Outline each blood parasite and name the species.
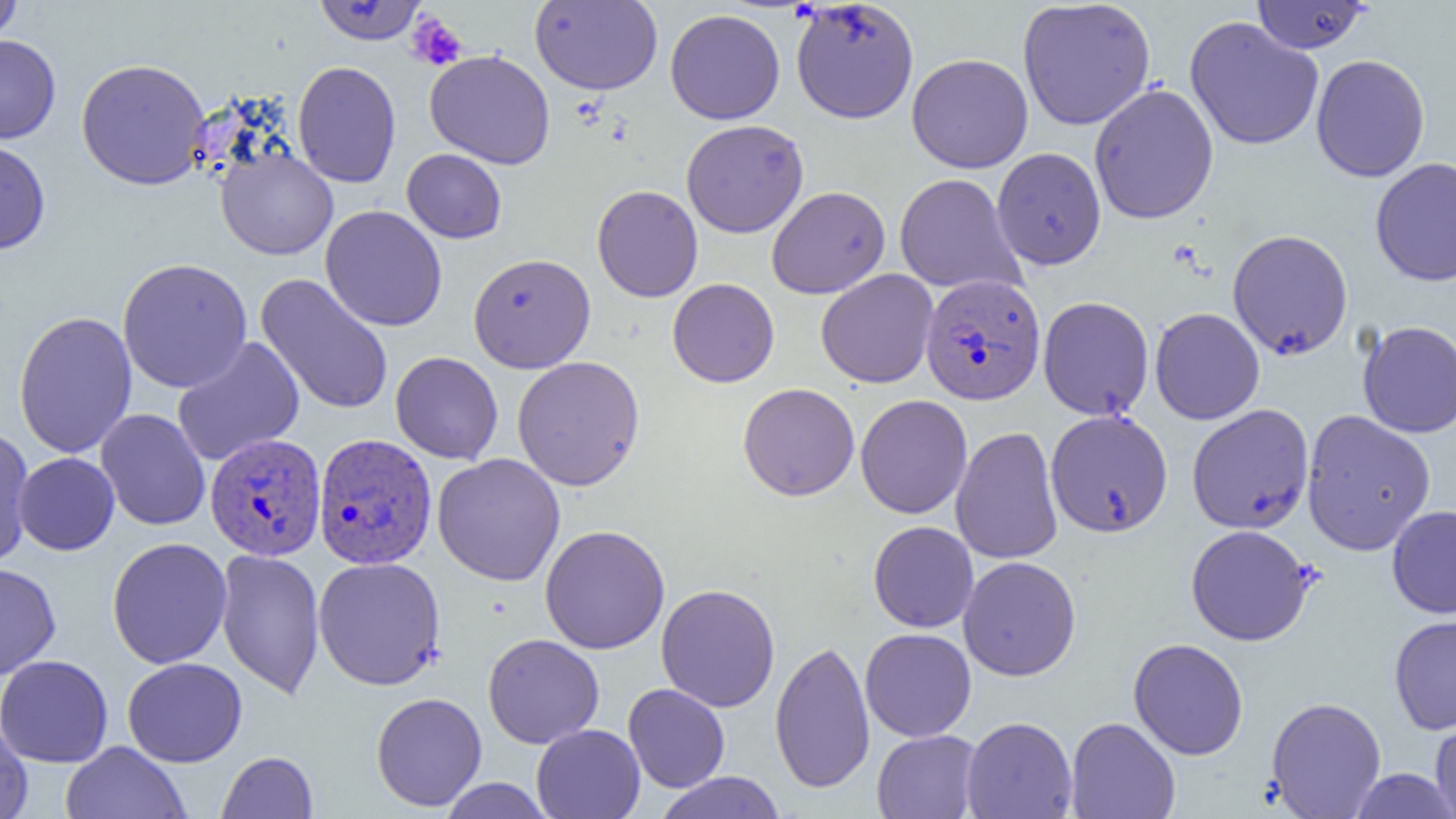

Approximate bounding boxes as named x1/y1/x2/y2 corners in pixels.
Plasmodium vivax-infected red blood cells: (x1=920, y1=274, x2=1046, y2=405), (x1=205, y1=433, x2=327, y2=561), (x1=313, y1=433, x2=437, y2=569).
No Plasmodium falciparum, Plasmodium ovale, Plasmodium malariae, Babesia divergens, or Trypanosoma brucei observed.

Uninfected red blood cell locations: (x1=0, y1=0, x2=22, y2=46), (x1=312, y1=0, x2=427, y2=44), (x1=530, y1=0, x2=663, y2=95), (x1=791, y1=1, x2=919, y2=123), (x1=1017, y1=1, x2=1156, y2=130), (x1=1250, y1=1, x2=1370, y2=53), (x1=665, y1=9, x2=785, y2=125), (x1=1184, y1=17, x2=1324, y2=150), (x1=0, y1=34, x2=61, y2=144), (x1=425, y1=50, x2=555, y2=170), (x1=906, y1=53, x2=1033, y2=173), (x1=1310, y1=54, x2=1430, y2=182), (x1=76, y1=58, x2=211, y2=190), (x1=292, y1=61, x2=402, y2=188), (x1=1089, y1=83, x2=1219, y2=224), (x1=681, y1=119, x2=809, y2=238), (x1=0, y1=138, x2=51, y2=255), (x1=216, y1=147, x2=338, y2=260), (x1=991, y1=147, x2=1106, y2=270), (x1=402, y1=149, x2=507, y2=243), (x1=1370, y1=157, x2=1456, y2=287), (x1=894, y1=173, x2=1025, y2=295), (x1=592, y1=185, x2=703, y2=302), (x1=767, y1=186, x2=891, y2=299), (x1=320, y1=205, x2=448, y2=331), (x1=1227, y1=228, x2=1353, y2=360), (x1=468, y1=252, x2=596, y2=373), (x1=117, y1=257, x2=253, y2=393), (x1=815, y1=269, x2=939, y2=388), (x1=256, y1=273, x2=395, y2=416), (x1=668, y1=278, x2=779, y2=387), (x1=1038, y1=296, x2=1154, y2=421), (x1=1150, y1=307, x2=1265, y2=424), (x1=13, y1=311, x2=138, y2=459), (x1=1357, y1=321, x2=1456, y2=437), (x1=172, y1=337, x2=305, y2=466), (x1=390, y1=351, x2=503, y2=464), (x1=512, y1=355, x2=645, y2=491), (x1=737, y1=383, x2=859, y2=500), (x1=855, y1=395, x2=972, y2=518), (x1=1187, y1=404, x2=1314, y2=534), (x1=96, y1=409, x2=211, y2=531), (x1=1045, y1=409, x2=1173, y2=537), (x1=1301, y1=410, x2=1436, y2=555), (x1=951, y1=426, x2=1064, y2=565), (x1=1, y1=428, x2=35, y2=565), (x1=13, y1=452, x2=119, y2=555), (x1=432, y1=453, x2=565, y2=586), (x1=1387, y1=505, x2=1456, y2=618), (x1=868, y1=521, x2=978, y2=633), (x1=540, y1=524, x2=670, y2=654), (x1=1185, y1=524, x2=1316, y2=646), (x1=106, y1=536, x2=232, y2=669), (x1=216, y1=548, x2=325, y2=700), (x1=959, y1=556, x2=1081, y2=681), (x1=313, y1=557, x2=446, y2=691), (x1=0, y1=563, x2=61, y2=679), (x1=656, y1=583, x2=780, y2=712), (x1=1389, y1=613, x2=1456, y2=735), (x1=860, y1=628, x2=976, y2=742), (x1=483, y1=633, x2=604, y2=749), (x1=1128, y1=638, x2=1249, y2=760), (x1=770, y1=639, x2=875, y2=794), (x1=0, y1=654, x2=113, y2=768), (x1=123, y1=657, x2=247, y2=767), (x1=623, y1=683, x2=730, y2=792), (x1=371, y1=692, x2=487, y2=811), (x1=1266, y1=696, x2=1386, y2=818), (x1=1431, y1=715, x2=1456, y2=818), (x1=961, y1=716, x2=1078, y2=819), (x1=1066, y1=716, x2=1180, y2=819), (x1=0, y1=717, x2=33, y2=819), (x1=532, y1=724, x2=646, y2=819), (x1=872, y1=729, x2=982, y2=819), (x1=60, y1=741, x2=191, y2=819), (x1=217, y1=751, x2=318, y2=818), (x1=1348, y1=768, x2=1456, y2=818), (x1=654, y1=771, x2=786, y2=819), (x1=439, y1=778, x2=555, y2=818). Platelet locations: (x1=407, y1=14, x2=466, y2=71). Slide-level diagnosis: Plasmodium vivax. Captured at 1000x magnification. Image is 1456×819 pixels. Optical microscopy. One field of a larger specimen. Thin blood smear.